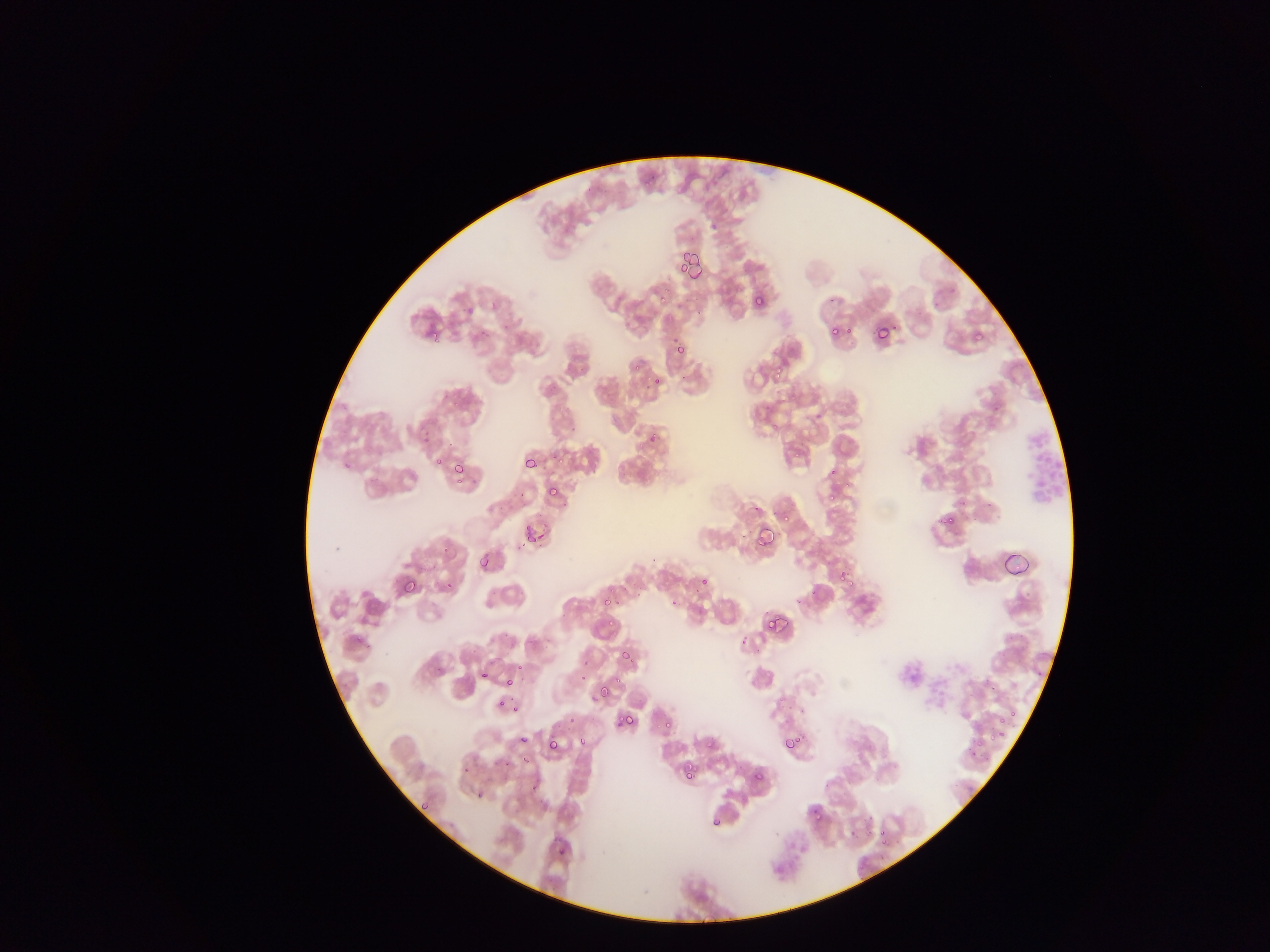

Approximate bounding boxes as left top right bottom in pixels.
Summary:
  - Plasmodium parasite locations: 679 257 698 277; 676 259 690 275; 658 292 670 305; 753 296 764 308; 463 299 474 319; 832 324 851 338; 873 324 889 343; 828 326 840 337; 972 330 983 340; 429 331 439 341; 666 337 690 361; 774 362 787 377; 651 376 661 386; 644 421 666 444; 523 456 538 470; 432 458 445 467; 342 462 350 470; 452 462 465 475; 454 473 463 486; 826 477 842 499; 546 485 557 496; 775 508 791 523; 939 510 956 527; 523 525 532 537; 756 527 774 546; 538 532 548 542; 1000 549 1033 576; 480 557 491 569; 838 569 856 591; 399 577 417 597; 701 577 709 585; 699 578 707 587; 443 581 453 590; 602 596 614 606; 669 598 679 607; 765 614 783 630; 609 618 618 629; 618 637 634 664; 513 661 523 671; 479 670 489 679; 505 676 516 688; 593 683 615 703; 496 697 508 708; 513 703 521 713; 616 712 632 726; 989 714 1009 749; 661 719 673 732; 965 728 984 750; 782 734 798 750; 519 735 528 744; 577 736 587 747; 705 738 716 749; 546 739 558 752; 500 758 510 768; 462 765 470 774; 683 769 695 780; 751 772 761 782; 475 791 484 800; 420 802 429 811; 810 806 822 818; 710 816 722 827; 878 828 887 839; 558 847 568 856
  - Leukocyte locations: 1020 423 1065 507
  - Capture: mobile-phone photograph through a microscope
  - Image size: 1270×952 pixels
  - Preparation: thin blood smear
  - Country: Ghana
  - Field of view: single